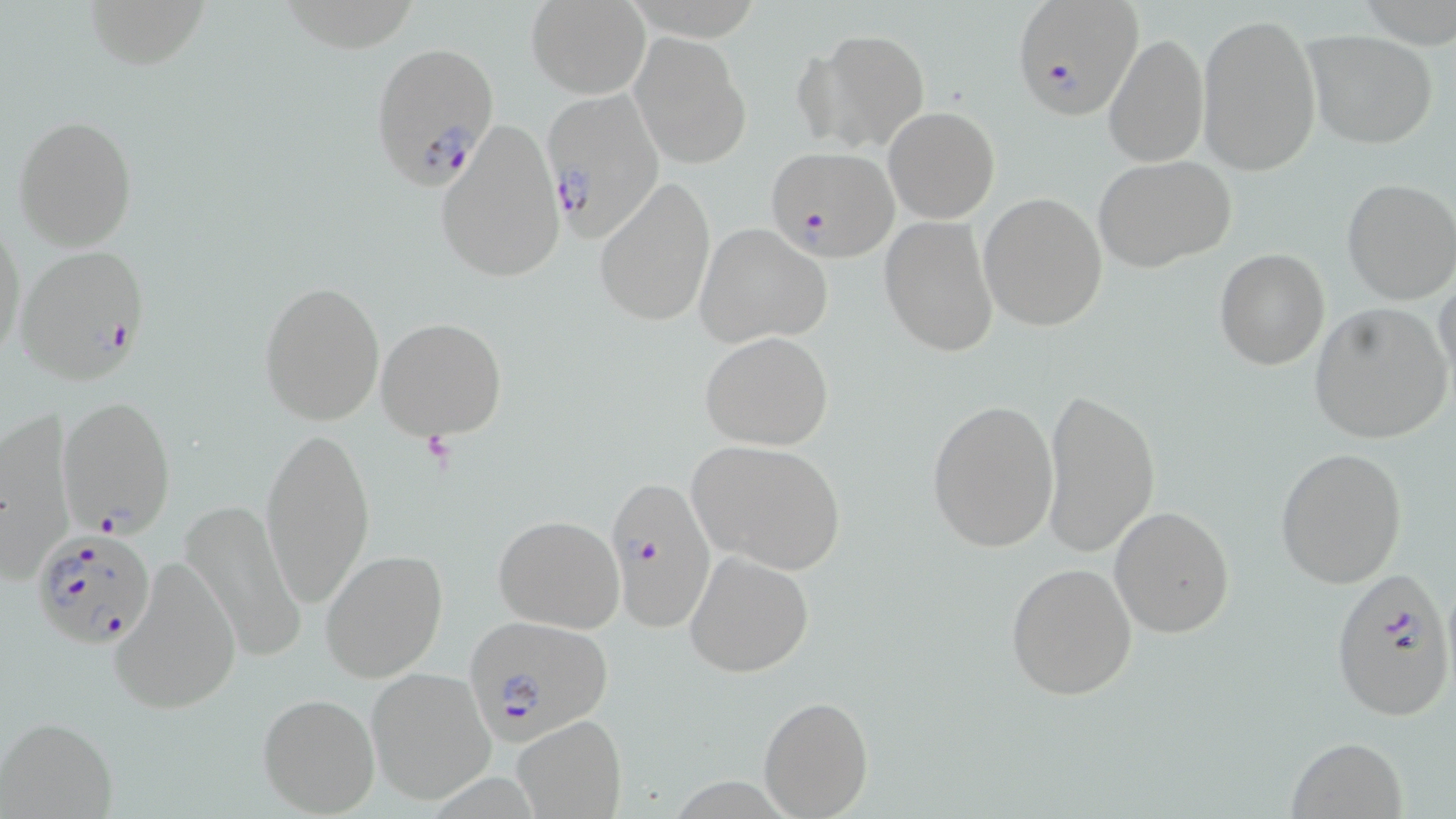
slide_level_diagnosis: Plasmodium falciparum
modality: optical microscopy
image_size: 1456×819 pixels
stain: May-Grünwald-Giemsa
preparation: thin blood film
magnification: 1000x
field_of_view: one of a larger specimen
uninfected_red_blood_cell_locations: 'approximate bounding boxes as (x1, y1, x2, y2) in pixels: (81, 0, 213, 69), (527, 1, 649, 98), (1198, 10, 1322, 176), (800, 29, 931, 153), (1102, 30, 1208, 167), (1304, 30, 1436, 148), (630, 33, 751, 169), (884, 106, 1000, 223), (13, 115, 138, 252), (433, 119, 565, 285), (1093, 156, 1238, 275), (594, 175, 717, 328), (1340, 177, 1456, 305), (978, 191, 1108, 332), (879, 215, 999, 358), (0, 216, 25, 365), (694, 223, 832, 347), (1214, 248, 1329, 370), (1435, 276, 1456, 393), (257, 278, 385, 427), (1310, 304, 1453, 443), (375, 316, 510, 441), (700, 330, 834, 451), (1040, 385, 1160, 559), (927, 398, 1058, 553), (0, 416, 75, 583), (260, 425, 376, 608), (686, 438, 847, 572), (1276, 446, 1406, 589), (182, 499, 308, 666), (1110, 505, 1235, 638), (493, 514, 624, 633), (320, 548, 449, 684), (684, 550, 814, 678), (108, 555, 242, 717), (1005, 562, 1138, 699), (364, 666, 495, 805), (258, 690, 380, 815), (758, 695, 874, 818), (514, 715, 627, 818), (2, 717, 117, 818), (1284, 736, 1408, 819)'
plasmodium_falciparum_infected_red_blood_cell_locations: 'approximate bounding boxes as (x1, y1, x2, y2) in pixels: (1012, 0, 1145, 122), (369, 41, 498, 188), (539, 87, 667, 239), (765, 146, 898, 261), (13, 243, 153, 384), (58, 396, 176, 539), (602, 470, 718, 637), (29, 526, 158, 649), (1330, 567, 1453, 723), (464, 616, 613, 745)'